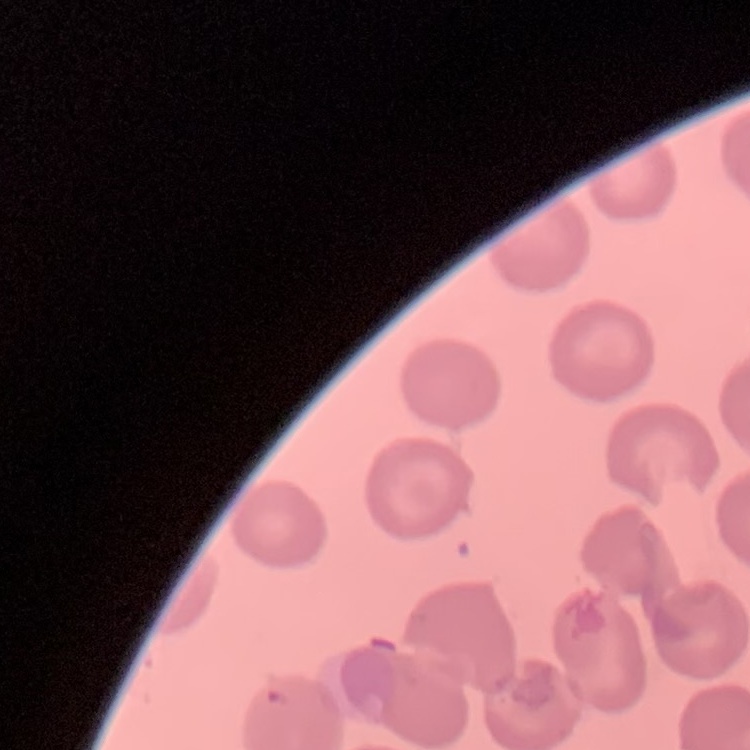 The erythrocytes show no rouleaux formation. Square crop of a larger photomicrograph. Thin blood smear. Field's or Giemsa stain.